Point out each malaria parasite.
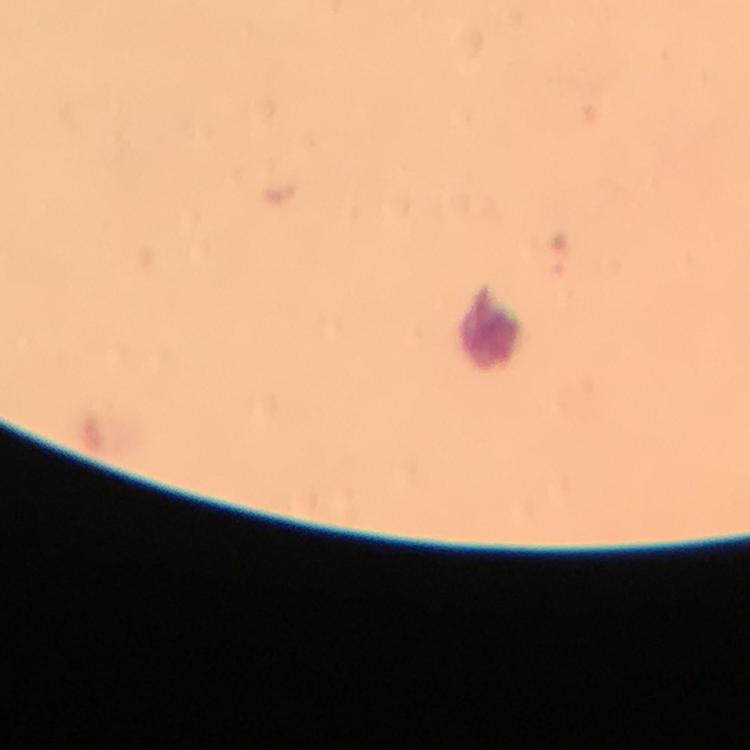
Approximate centers as (x, y) in pixels.
Malaria parasites: (558, 257).

immersion oil = applied
stain = Giemsa
leukocyte locations = approximate centers as (x, y) in pixels: (489, 328)
cropped from = a single field of view
capture = smartphone mounted on the microscope
context = from a diagnostic examination for malaria
preparation = thick blood film
image size = 750×750 pixels
magnification = 100x